Assess this cell for malaria.
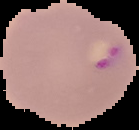
Parasitized.

Segmented cell region on a black background. From a thin blood film. Image is 139×130 pixels.